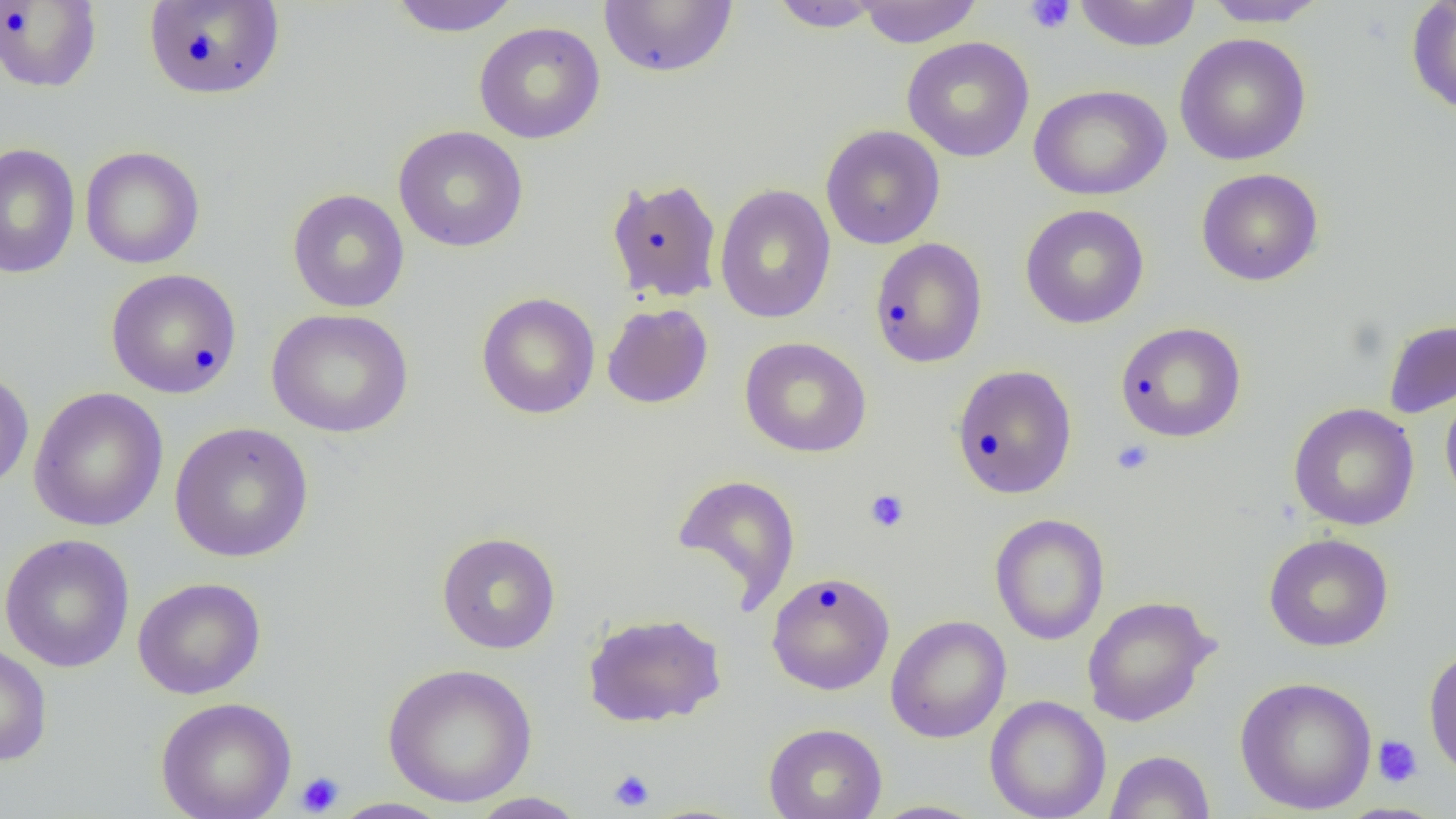

{
  "slide_level_diagnosis": "negative for blood parasites",
  "platelet_locations": "approximate bounding boxes as named x1/y1/x2/y2 corners in pixels: (x1=1024, y1=0, x2=1076, y2=34), (x1=1111, y1=439, x2=1154, y2=475), (x1=865, y1=489, x2=909, y2=533), (x1=1372, y1=735, x2=1423, y2=788), (x1=608, y1=769, x2=655, y2=812), (x1=295, y1=772, x2=344, y2=816)",
  "preparation": "thin blood film",
  "field_of_view": "single",
  "image_size": "1456×819 pixels",
  "modality": "optical microscopy",
  "magnification": "1000x",
  "uninfected_red_blood_cell_locations": "approximate bounding boxes as named x1/y1/x2/y2 corners in pixels: (x1=143, y1=0, x2=285, y2=99), (x1=386, y1=0, x2=522, y2=37), (x1=599, y1=0, x2=738, y2=78), (x1=854, y1=0, x2=983, y2=47), (x1=1072, y1=0, x2=1202, y2=51), (x1=1201, y1=0, x2=1331, y2=28), (x1=1406, y1=0, x2=1456, y2=117), (x1=0, y1=1, x2=102, y2=92), (x1=767, y1=1, x2=887, y2=32), (x1=473, y1=21, x2=606, y2=144), (x1=1174, y1=32, x2=1312, y2=166), (x1=901, y1=36, x2=1035, y2=162), (x1=1028, y1=84, x2=1171, y2=201), (x1=393, y1=125, x2=529, y2=252), (x1=820, y1=125, x2=945, y2=249), (x1=0, y1=143, x2=81, y2=279), (x1=80, y1=146, x2=205, y2=269), (x1=1196, y1=168, x2=1324, y2=286), (x1=606, y1=178, x2=723, y2=304), (x1=714, y1=184, x2=836, y2=324), (x1=287, y1=188, x2=409, y2=313), (x1=1020, y1=204, x2=1149, y2=329), (x1=869, y1=237, x2=988, y2=368), (x1=106, y1=268, x2=242, y2=399), (x1=476, y1=292, x2=600, y2=419), (x1=602, y1=303, x2=713, y2=409), (x1=266, y1=308, x2=414, y2=438), (x1=1382, y1=318, x2=1456, y2=419), (x1=1115, y1=322, x2=1247, y2=442), (x1=739, y1=337, x2=871, y2=458), (x1=951, y1=364, x2=1078, y2=499), (x1=0, y1=369, x2=34, y2=494), (x1=28, y1=386, x2=168, y2=532), (x1=1440, y1=386, x2=1456, y2=509), (x1=1288, y1=402, x2=1420, y2=531), (x1=169, y1=421, x2=314, y2=563), (x1=671, y1=473, x2=801, y2=612), (x1=989, y1=513, x2=1109, y2=645), (x1=436, y1=531, x2=561, y2=653), (x1=0, y1=533, x2=135, y2=673), (x1=1263, y1=533, x2=1394, y2=651), (x1=766, y1=571, x2=895, y2=695), (x1=132, y1=577, x2=267, y2=699), (x1=1081, y1=595, x2=1218, y2=727), (x1=582, y1=612, x2=726, y2=727), (x1=885, y1=615, x2=1011, y2=743), (x1=0, y1=641, x2=53, y2=766), (x1=1423, y1=645, x2=1456, y2=779), (x1=382, y1=662, x2=538, y2=807), (x1=1234, y1=676, x2=1377, y2=815), (x1=985, y1=695, x2=1110, y2=819), (x1=156, y1=696, x2=296, y2=819), (x1=763, y1=722, x2=887, y2=819), (x1=1105, y1=750, x2=1215, y2=818), (x1=465, y1=792, x2=590, y2=818), (x1=329, y1=798, x2=452, y2=819), (x1=868, y1=800, x2=989, y2=818)"
}